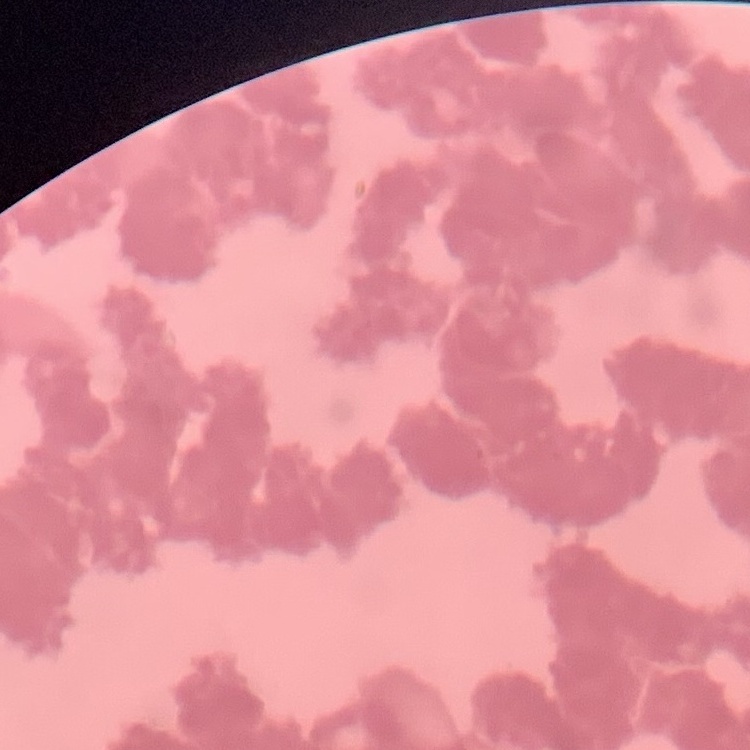

erythrocyte morphology = rouleaux formation
stain = Field's or Giemsa
preparation = thin blood smear
image type = one tile cut from a larger photomicrograph